Assess the morphology of the erythrocytes.
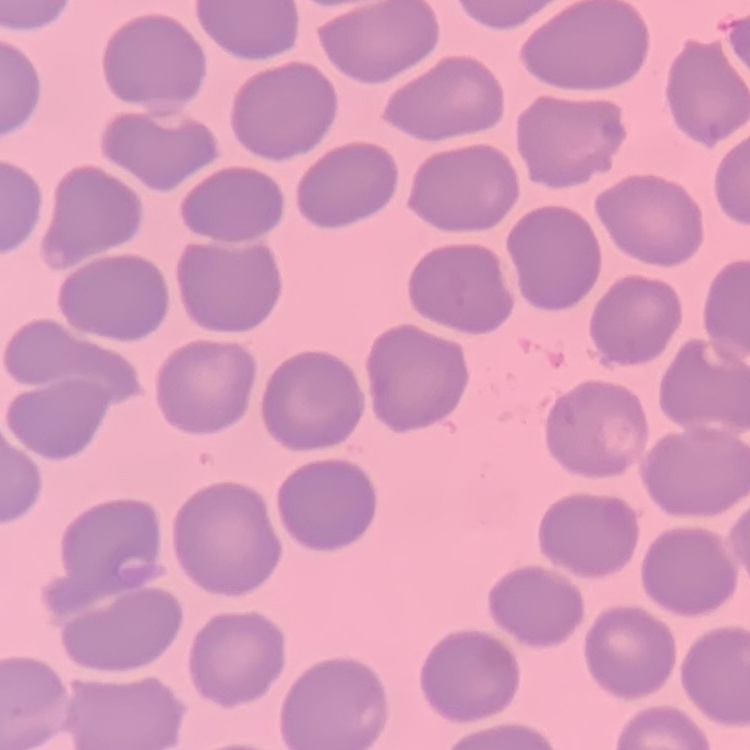

They show no rouleaux formation.

preparation = thin blood film
stain = Field's or Giemsa
image type = square crop of a larger photomicrograph